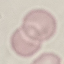

Summary:
  - Malaria status: uninfected
  - Image type: cell patch, automatically extracted from a larger field of view and resized to 64 × 64 pixels
  - Stain: Giemsa
  - Capture: smartphone camera at the microscope eyepiece
  - Preparation: thin smear